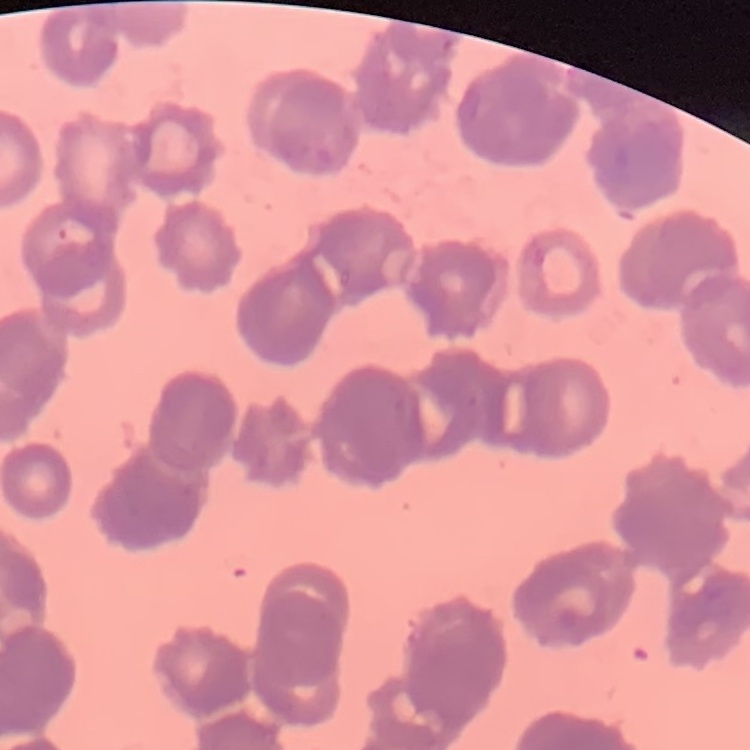

Summary:
  - Erythrocyte morphology: rouleaux formation
  - Stain: Field's or Giemsa
  - Image type: one tile cut from a larger photomicrograph
  - Preparation: thin peripheral smear